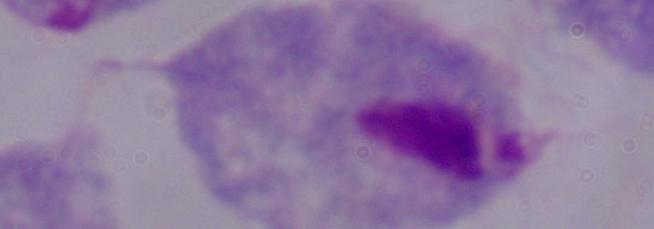
Summary:
  - Modality: micrograph
  - Magnification: 1000x
  - Identification: trichomonad